Assess the morphology of the red blood cells.
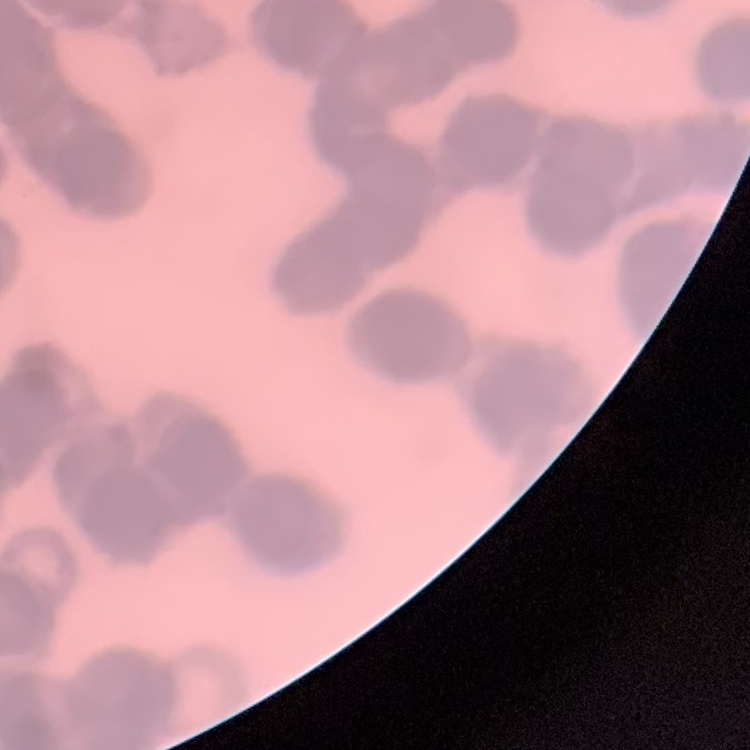
Rouleaux formation.

{
  "image_type": "square crop of a larger photomicrograph",
  "stain": "Field's or Giemsa",
  "preparation": "thin blood smear"
}